Classify this cell by malaria status.
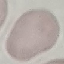
Uninfected.

stain = Giemsa
image type = cell patch, automatically extracted from a larger field of view and resized to 64 × 64 pixels
capture = smartphone through the microscope eyepiece
preparation = thin blood smear